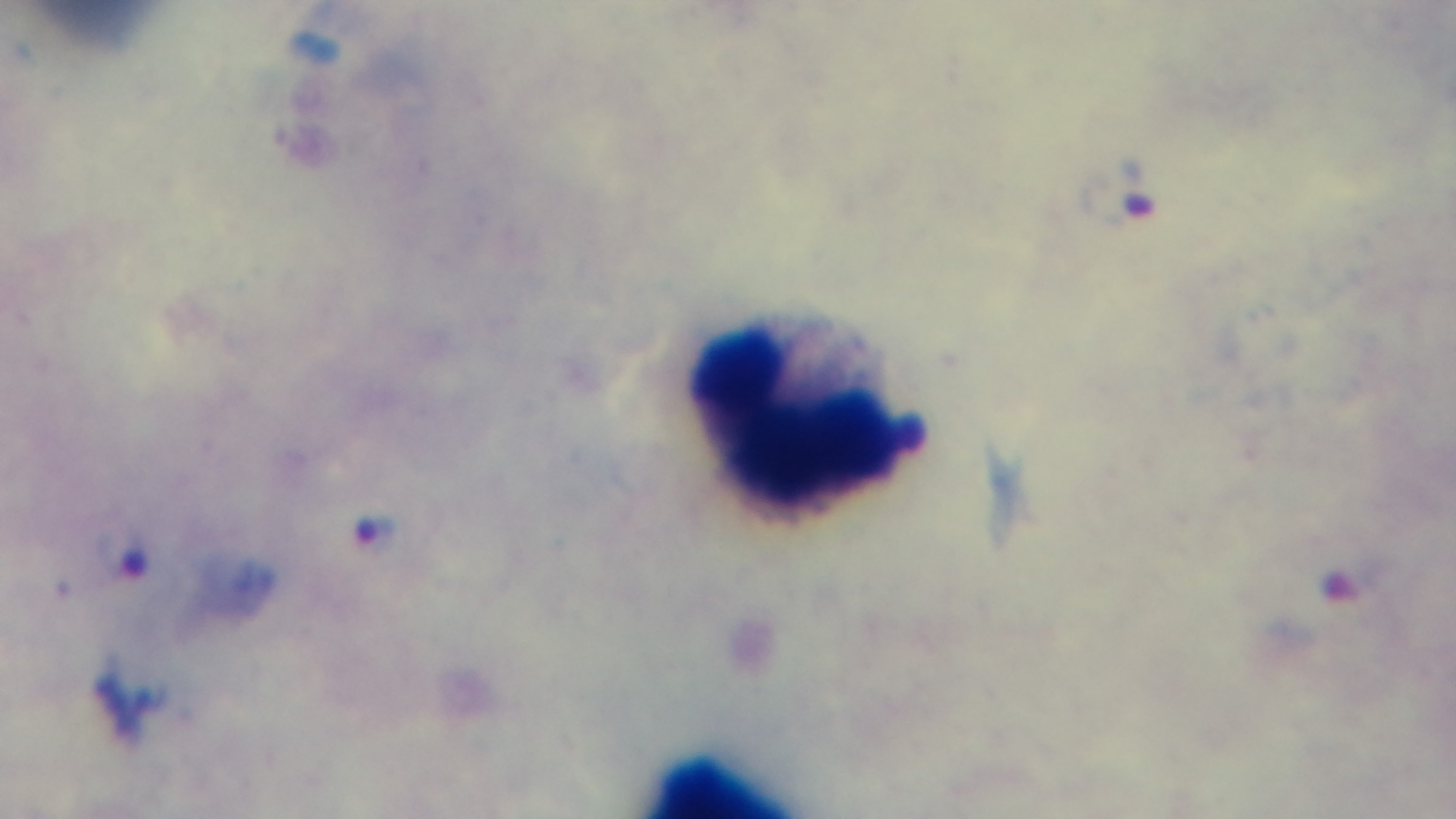

stain = Giemsa
objective = 100x oil immersion
preparation = thick smear
field of view = one from the slide
malaria status = infected
capture = mounted 4K digital camera
modality = light microscopy